Assess this cell for malaria.
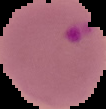

It is parasitized.

Summary:
  - Preparation: thin blood film
  - Image type: segmented cell region on a black background
  - Image size: 106×109 pixels